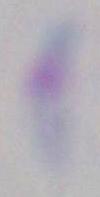

{
  "magnification": "1000x",
  "identification": "Toxoplasma gondii",
  "modality": "micrograph"
}